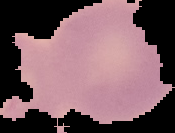
Image is 175×133 pixels. From a thin blood smear. Result: no Plasmodium parasites detected. The area outside the segmented cell region is set to black.